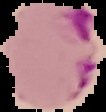
Malaria status: parasitized. Segmented cell region on a black background. Image is 106×112 pixels. From a thin blood film.